Assess this cell for malaria.
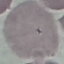
It is uninfected.

capture = smartphone camera at the microscope eyepiece
preparation = thin smear
image type = cell patch, automatically extracted from a larger field of view and resized to 64 × 64 pixels
stain = Giemsa